Comment on the morphology of the red blood cells.
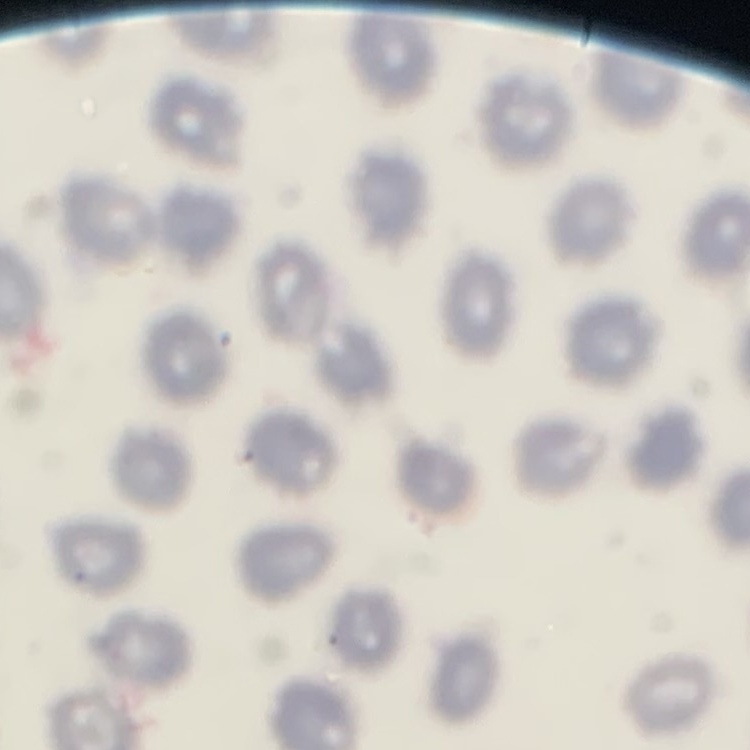
No rouleaux formation.

preparation = thin blood film
stain = Field's or Giemsa
image type = one tile cut from a larger photomicrograph